Classify this cell by malaria status.
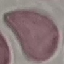

It is uninfected.

Thin smear of blood. Giemsa-stained preparation. Photographed with a smartphone camera at the microscope eyepiece. Automatically extracted cell patch, resized to 64 × 64 pixels.